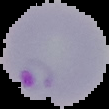
preparation = thin blood smear
image type = segmented cell region with the area outside set to black
image size = 109×109 pixels
result = malaria parasites detected